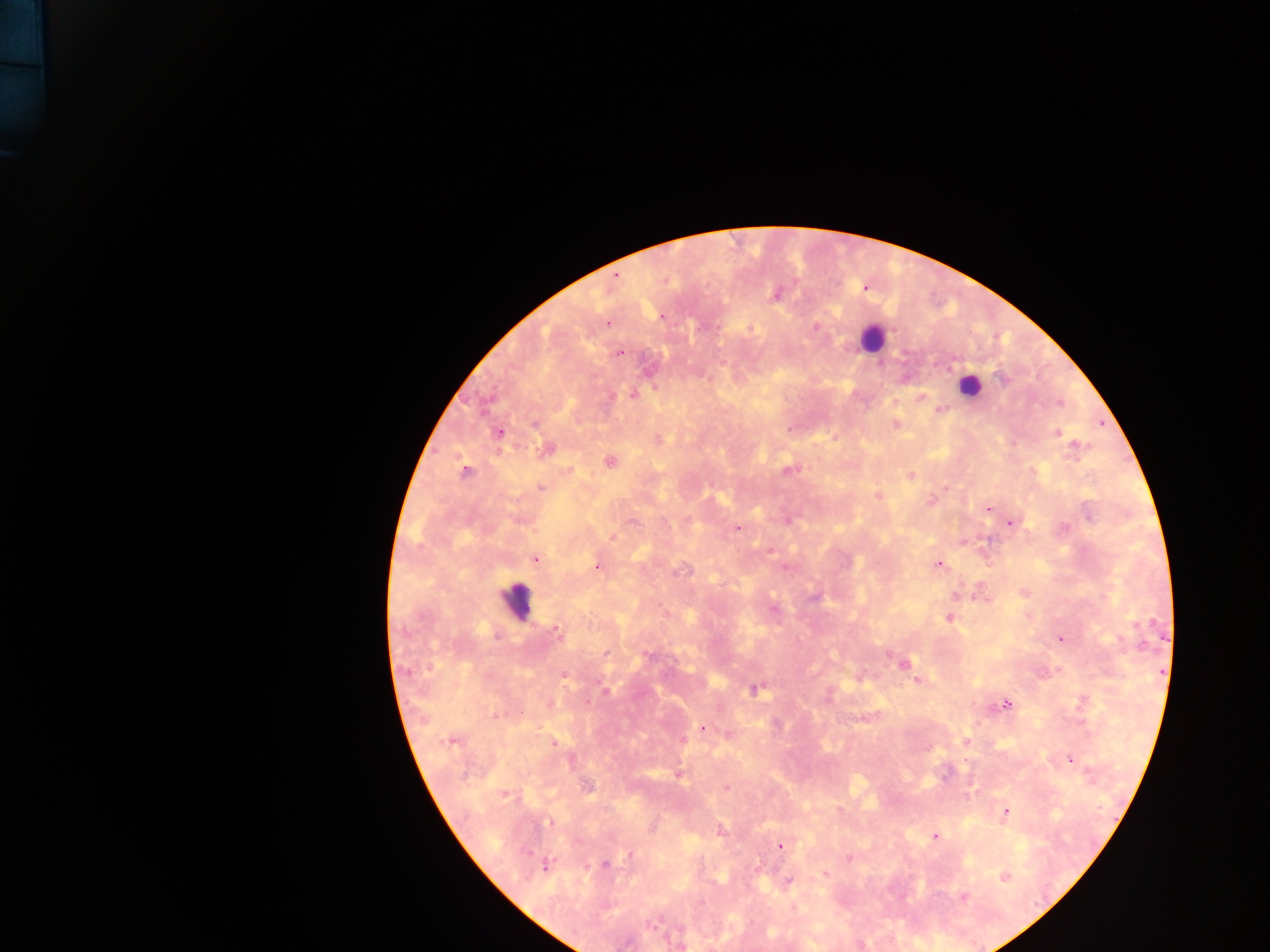
Approximate centers as x y in pixels.
Summary:
  - Leukocyte locations: 877 340; 969 387; 520 599
  - Malaria parasite locations: 616 275; 774 293; 661 317; 606 322; 815 327; 751 328; 619 353; 632 392; 918 397; 940 408; 534 423; 895 423; 1056 433; 657 439; 546 446; 609 461; 788 468; 463 469; 910 474; 541 487; 878 495; 929 498; 987 509; 1010 522; 736 528; 613 536; 534 559; 938 564; 596 566; 679 572; 1023 593; 774 600; 775 608; 949 618; 556 630; 1059 640; 609 653; 646 659; 905 660; 564 677; 917 679; 755 689; 606 692; 1006 703; 703 727; 727 734; 966 741; 553 742; 929 748; 1070 758; 679 772; 726 787; 504 795; 1005 812; 548 823; 653 829; 718 832; 936 836; 781 846; 629 856; 847 857; 546 865; 605 865; 758 865; 824 872; 1005 877; 788 881; 962 898; 793 907; 860 944; 681 945
  - Capture: mobile-phone photograph through a microscope
  - Field of view: single
  - Country: Ghana
  - Image size: 1270×952 pixels
  - Preparation: thick blood smear